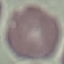

Summary:
  - Malaria status: uninfected
  - Capture: smartphone camera at the microscope eyepiece
  - Preparation: thin blood film
  - Image type: automatically extracted cell patch, resized to 64 × 64 pixels
  - Stain: Giemsa